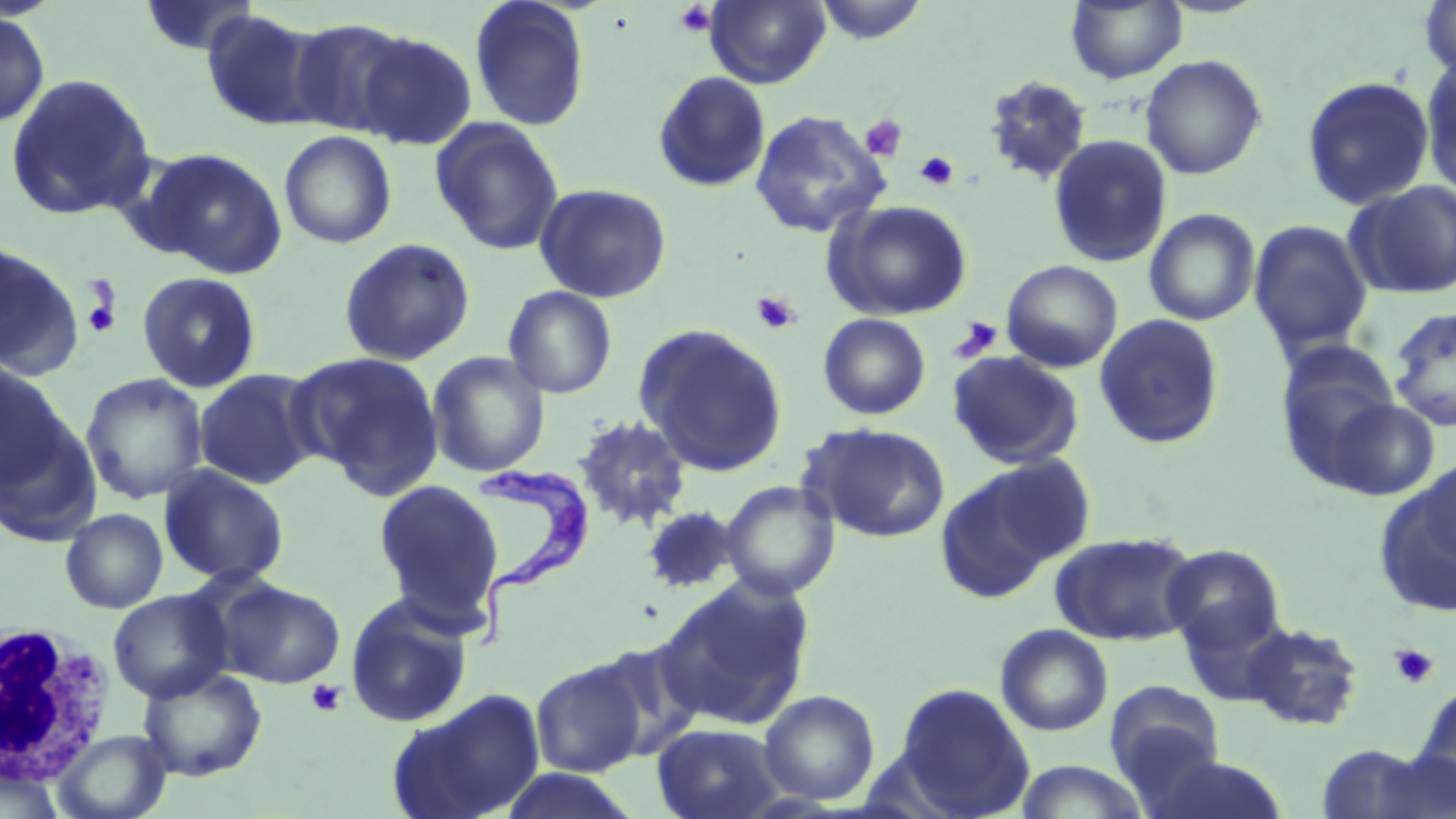

Approximate bounding boxes as (x1,y1)-(x2,y2) corner pairs in pixels. Trypanosoma brucei locations: (476,451)-(596,652). White blood cell locations: (0,622)-(116,785). Platelet locations: (673,2)-(717,38), (860,115)-(907,161), (915,151)-(960,191), (80,280)-(123,339), (751,291)-(802,334), (950,316)-(1003,362), (1389,643)-(1438,689), (306,679)-(346,717). Uninfected red blood cell locations: (137,0)-(260,57), (469,0)-(591,132), (705,0)-(831,88), (813,0)-(930,44), (1418,0)-(1456,80), (1065,1)-(1187,84), (201,10)-(326,131), (0,11)-(50,127), (288,18)-(414,137), (353,30)-(478,150), (1140,54)-(1267,180), (1420,56)-(1456,199), (653,71)-(771,193), (4,73)-(157,221), (983,74)-(1094,186), (1300,75)-(1435,211), (749,109)-(891,239), (429,117)-(565,256), (279,130)-(397,249), (1047,134)-(1173,268), (138,147)-(288,278), (1345,181)-(1456,300), (534,182)-(672,303), (822,199)-(973,321), (1144,208)-(1261,326), (1248,219)-(1374,357), (337,237)-(477,367), (0,242)-(83,380), (1001,259)-(1123,372), (137,271)-(262,393), (502,286)-(618,398), (1388,305)-(1456,433), (818,313)-(931,420), (1093,313)-(1226,449), (636,323)-(788,476), (1277,341)-(1402,464), (427,351)-(550,477), (948,351)-(1085,470), (290,352)-(445,497), (0,361)-(71,491), (193,368)-(322,490), (81,372)-(209,505), (1320,397)-(1440,501), (573,414)-(692,532), (0,416)-(101,548), (803,422)-(951,542), (1411,455)-(1456,576), (934,459)-(1079,603), (158,464)-(290,587), (1377,466)-(1456,616), (372,479)-(507,632), (720,480)-(840,600), (640,505)-(742,594), (60,508)-(168,614), (1051,531)-(1199,645), (1161,544)-(1285,653), (655,575)-(816,731), (217,579)-(345,688), (108,589)-(232,704), (344,592)-(474,729), (1175,597)-(1290,707), (1242,621)-(1365,732), (995,623)-(1114,737), (585,638)-(706,760), (529,657)-(648,777), (137,666)-(268,782), (1104,680)-(1226,798), (892,682)-(1036,818), (1413,684)-(1456,804), (386,688)-(547,819), (759,689)-(880,806), (652,723)-(786,819), (54,730)-(172,819), (1314,743)-(1442,819), (1144,753)-(1292,819), (1014,760)-(1151,819), (1,761)-(65,819), (496,768)-(645,819). Slide-level diagnosis: Trypanosoma brucei. 1000x magnification. Image is 1456×819 pixels. May-Grünwald-Giemsa-stained preparation. Single field of view. Thin blood smear. Light microscopy.